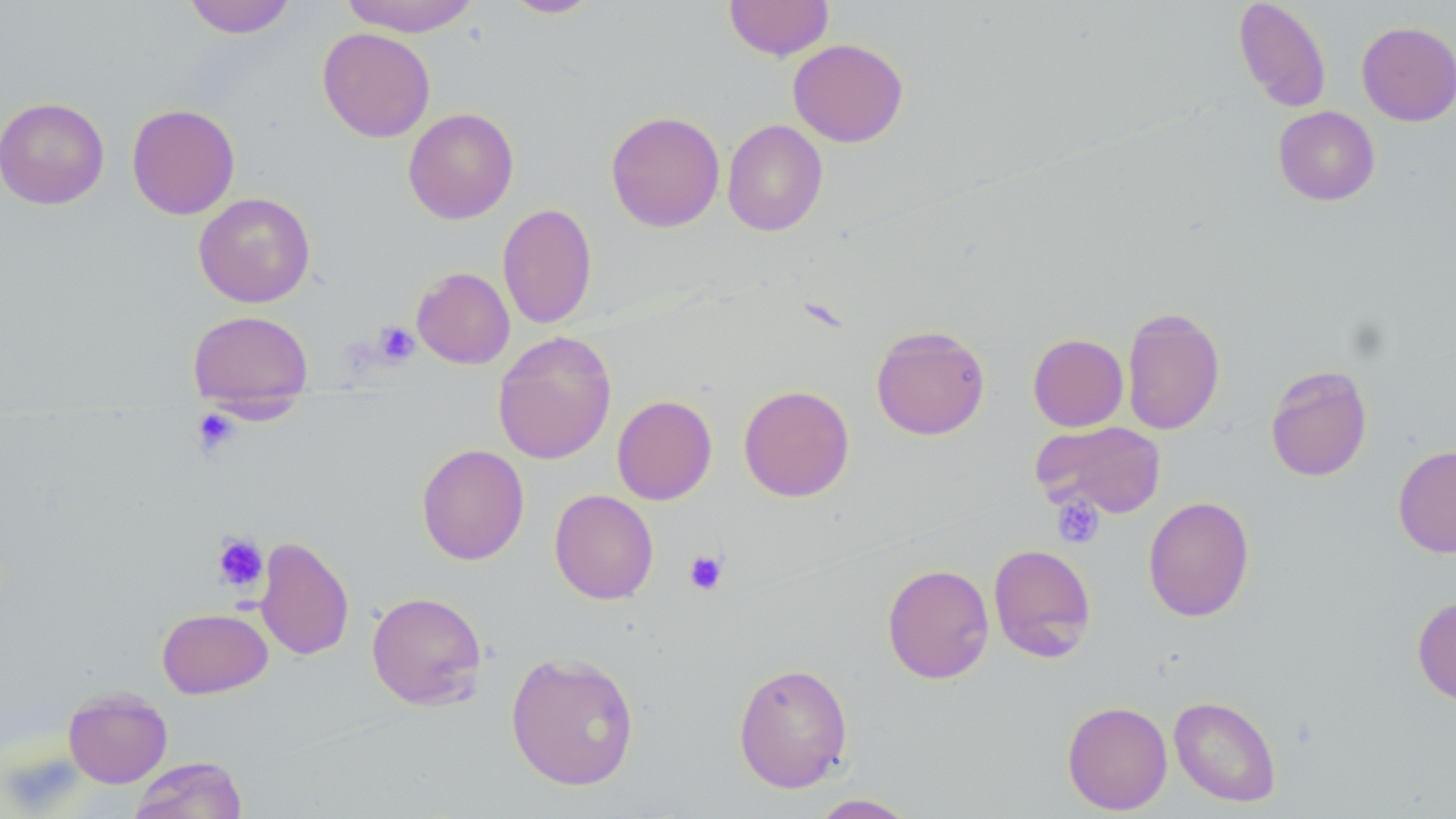

Summary:
  - Coordinate format: approximate bounding boxes as (x1,y1)-(x2,y2) corner pairs in pixels
  - Uninfected red blood cell locations: (182,0)-(296,38), (339,0)-(480,37), (501,0)-(602,18), (724,0)-(834,60), (1233,0)-(1331,113), (1357,21)-(1456,126), (318,27)-(435,142), (788,39)-(908,147), (0,96)-(110,209), (126,103)-(240,219), (1273,106)-(1380,206), (403,107)-(519,224), (605,110)-(725,233), (722,119)-(828,236), (193,192)-(315,307), (498,203)-(597,328), (411,267)-(515,369), (1122,306)-(1225,435), (187,310)-(313,405), (870,324)-(990,440), (493,331)-(617,465), (1028,333)-(1128,432), (1265,364)-(1373,482), (739,385)-(855,502), (612,395)-(717,505), (1032,421)-(1167,519), (416,443)-(529,565), (1393,444)-(1456,558), (549,489)-(659,604), (1142,496)-(1255,622), (255,536)-(354,661), (988,543)-(1097,662), (882,563)-(994,684), (366,591)-(488,710), (1412,595)-(1456,705), (157,607)-(272,698), (505,651)-(640,791), (733,661)-(853,793), (63,686)-(173,788), (1169,695)-(1281,807), (1062,701)-(1173,814), (128,756)-(248,818), (807,793)-(919,818)
  - Platelet locations: (373,321)-(419,367), (191,408)-(240,457), (1052,495)-(1104,548), (212,533)-(268,593), (684,550)-(728,595)
  - Slide-level diagnosis: no evidence of blood parasites
  - Stain: May-Grünwald-Giemsa
  - Magnification: 1000x
  - Preparation: thin blood film
  - Image size: 1456×819 pixels
  - Field of view: single
  - Modality: optical microscopy